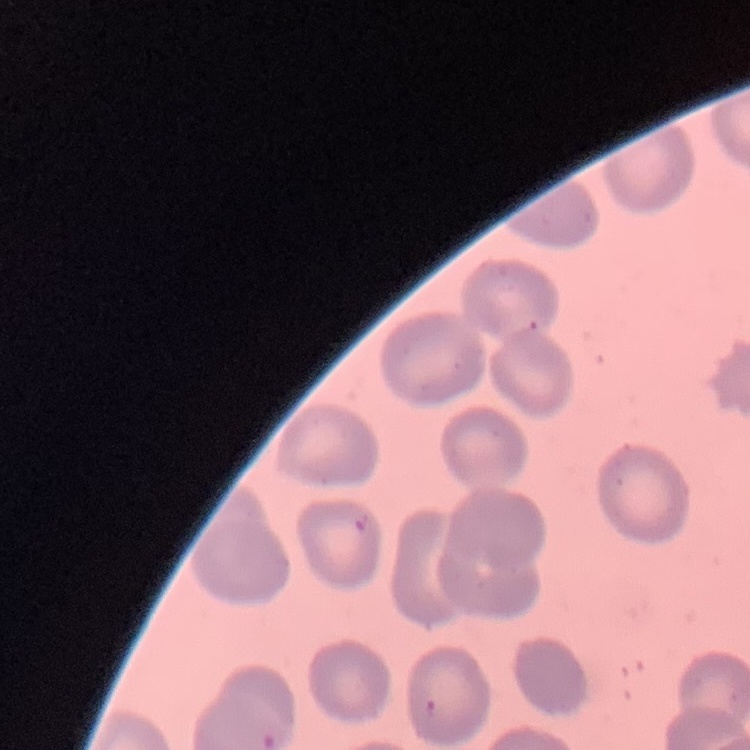 The red blood cells exhibit no rouleaux formation. Field's or Giemsa stain. Thin peripheral smear. One tile cut from a larger photomicrograph.